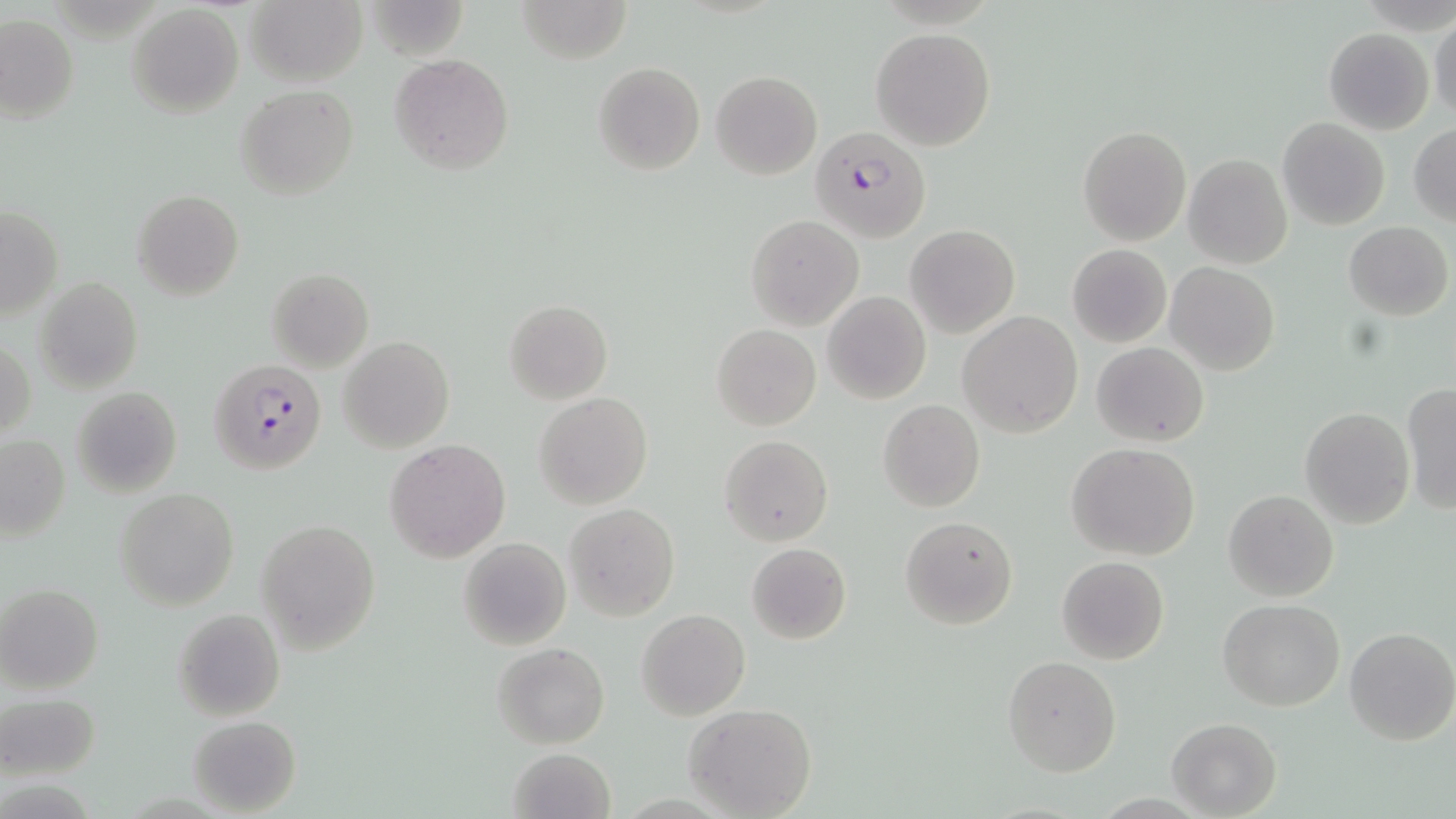

{
  "slide_level_diagnosis": "Plasmodium falciparum",
  "image_size": "1456×819 pixels",
  "modality": "light microscopy",
  "magnification": "1000x",
  "field_of_view": "one of a larger specimen",
  "preparation": "thin blood smear",
  "plasmodium_falciparum_infected_red_blood_cell_locations": "approximate bounding boxes as named x1/y1/x2/y2 corners in pixels: (x1=803, y1=125, x2=931, y2=245), (x1=210, y1=359, x2=326, y2=476)",
  "uninfected_red_blood_cell_locations": "approximate bounding boxes as named x1/y1/x2/y2 corners in pixels: (x1=362, y1=0, x2=468, y2=60), (x1=516, y1=0, x2=633, y2=64), (x1=246, y1=1, x2=366, y2=87), (x1=126, y1=4, x2=244, y2=118), (x1=0, y1=13, x2=79, y2=122), (x1=1429, y1=14, x2=1456, y2=121), (x1=871, y1=27, x2=997, y2=150), (x1=1323, y1=28, x2=1434, y2=134), (x1=389, y1=53, x2=514, y2=173), (x1=593, y1=62, x2=706, y2=175), (x1=710, y1=70, x2=822, y2=180), (x1=235, y1=85, x2=359, y2=198), (x1=1278, y1=118, x2=1390, y2=231), (x1=1409, y1=123, x2=1456, y2=227), (x1=1078, y1=126, x2=1191, y2=245), (x1=1183, y1=154, x2=1293, y2=269), (x1=133, y1=190, x2=243, y2=300), (x1=1, y1=206, x2=63, y2=319), (x1=746, y1=214, x2=864, y2=331), (x1=1343, y1=221, x2=1452, y2=319), (x1=906, y1=224, x2=1019, y2=338), (x1=1066, y1=245, x2=1171, y2=347), (x1=1167, y1=263, x2=1279, y2=374), (x1=267, y1=269, x2=373, y2=372), (x1=33, y1=277, x2=143, y2=392), (x1=823, y1=292, x2=931, y2=406), (x1=504, y1=300, x2=613, y2=404), (x1=957, y1=311, x2=1084, y2=437), (x1=713, y1=324, x2=821, y2=430), (x1=1, y1=336, x2=35, y2=443), (x1=339, y1=337, x2=454, y2=454), (x1=1091, y1=342, x2=1208, y2=447), (x1=1401, y1=383, x2=1456, y2=515), (x1=71, y1=388, x2=182, y2=497), (x1=535, y1=393, x2=652, y2=509), (x1=878, y1=399, x2=986, y2=512), (x1=1300, y1=408, x2=1414, y2=529), (x1=0, y1=434, x2=70, y2=543), (x1=719, y1=435, x2=833, y2=545), (x1=385, y1=439, x2=510, y2=564), (x1=1067, y1=443, x2=1201, y2=562), (x1=114, y1=488, x2=241, y2=611), (x1=1223, y1=489, x2=1339, y2=601), (x1=565, y1=502, x2=680, y2=621), (x1=899, y1=515, x2=1017, y2=629), (x1=256, y1=519, x2=381, y2=653), (x1=458, y1=537, x2=571, y2=650), (x1=746, y1=544, x2=850, y2=643), (x1=1056, y1=556, x2=1169, y2=665), (x1=0, y1=583, x2=104, y2=695), (x1=1218, y1=598, x2=1345, y2=711), (x1=171, y1=608, x2=285, y2=722), (x1=635, y1=609, x2=750, y2=720), (x1=1344, y1=627, x2=1456, y2=746), (x1=493, y1=642, x2=609, y2=748), (x1=1002, y1=655, x2=1121, y2=776), (x1=1, y1=692, x2=102, y2=781), (x1=684, y1=702, x2=818, y2=818), (x1=188, y1=715, x2=300, y2=815), (x1=1166, y1=717, x2=1283, y2=817), (x1=507, y1=747, x2=615, y2=819)",
  "stain": "May-Grünwald-Giemsa"
}